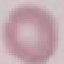

result: negative for malaria parasites
preparation: thin smear
image_type: automatically extracted cell patch, resized to 64 × 64 pixels
capture: smartphone camera at the microscope eyepiece
stain: Giemsa